Assess this cell for malaria.
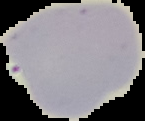

Uninfected.

Summary:
  - Image type: segmented cell region on a black background
  - Preparation: thin blood smear
  - Image size: 145×121 pixels